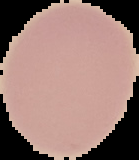
Malaria status: uninfected. Image is 139×160 pixels. Segmented cell region on a black background. From a thin blood film.